State which parasite is depicted.
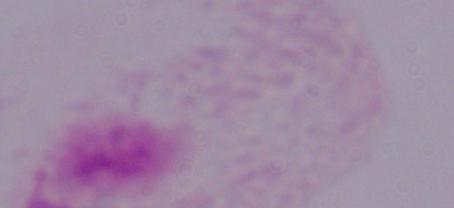
A trichomonad.

modality = micrograph
magnification = 1000x